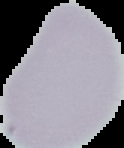

From a thin blood smear. Segmented cell region on a black background. Image is 124×148 pixels. Result: negative for malaria parasites.